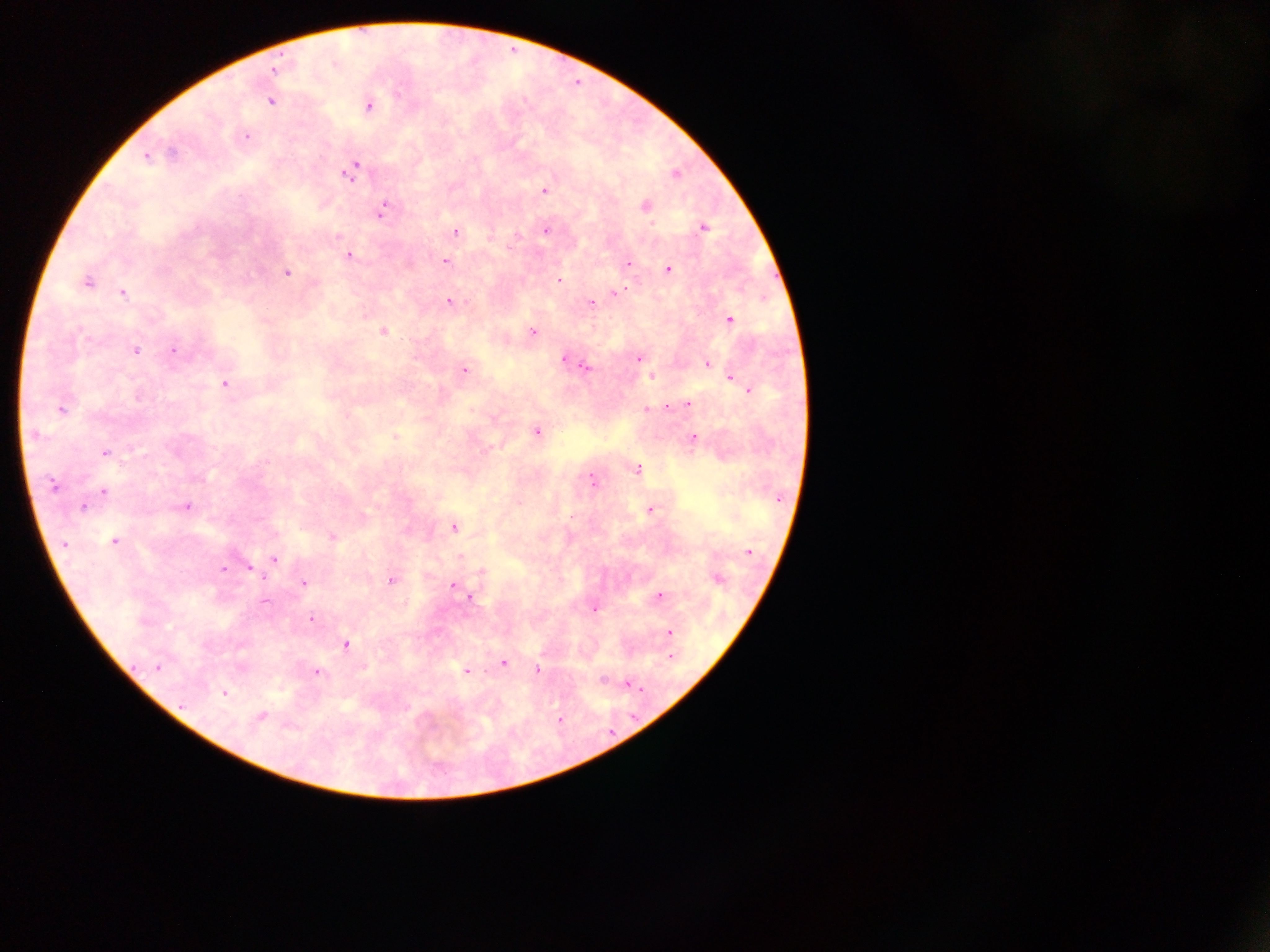 Approximate centers as x y in pixels. Plasmodium parasite locations: 275 70; 270 100; 368 105; 245 137; 146 156; 351 171; 675 174; 544 190; 644 206; 382 210; 703 227; 546 230; 455 232; 348 256; 444 262; 628 264; 668 269; 286 272; 558 280; 86 282; 123 292; 615 293; 449 301; 592 303; 728 319; 383 331; 533 332; 134 349; 172 350; 564 359; 638 359; 572 361; 707 363; 464 369; 586 369; 651 376; 730 377; 225 384; 749 390; 687 403; 60 407; 646 407; 536 431; 693 438; 104 453; 636 469; 592 480; 53 485; 103 491; 518 503; 83 505; 185 506; 650 509; 453 526; 332 537; 114 541; 63 544; 748 551; 273 558; 249 566; 223 567; 481 571; 717 579; 391 581; 303 582; 452 585; 657 596; 470 597; 593 607; 312 618; 669 631; 345 645; 670 655; 503 662; 157 667; 466 670; 537 670; 316 671; 627 683; 223 692; 260 717; 559 719. One field of view. Image is 1270×952 pixels. Photographed through a microscope with a mobile-phone camera. Thick blood smear. Collected in Ghana.